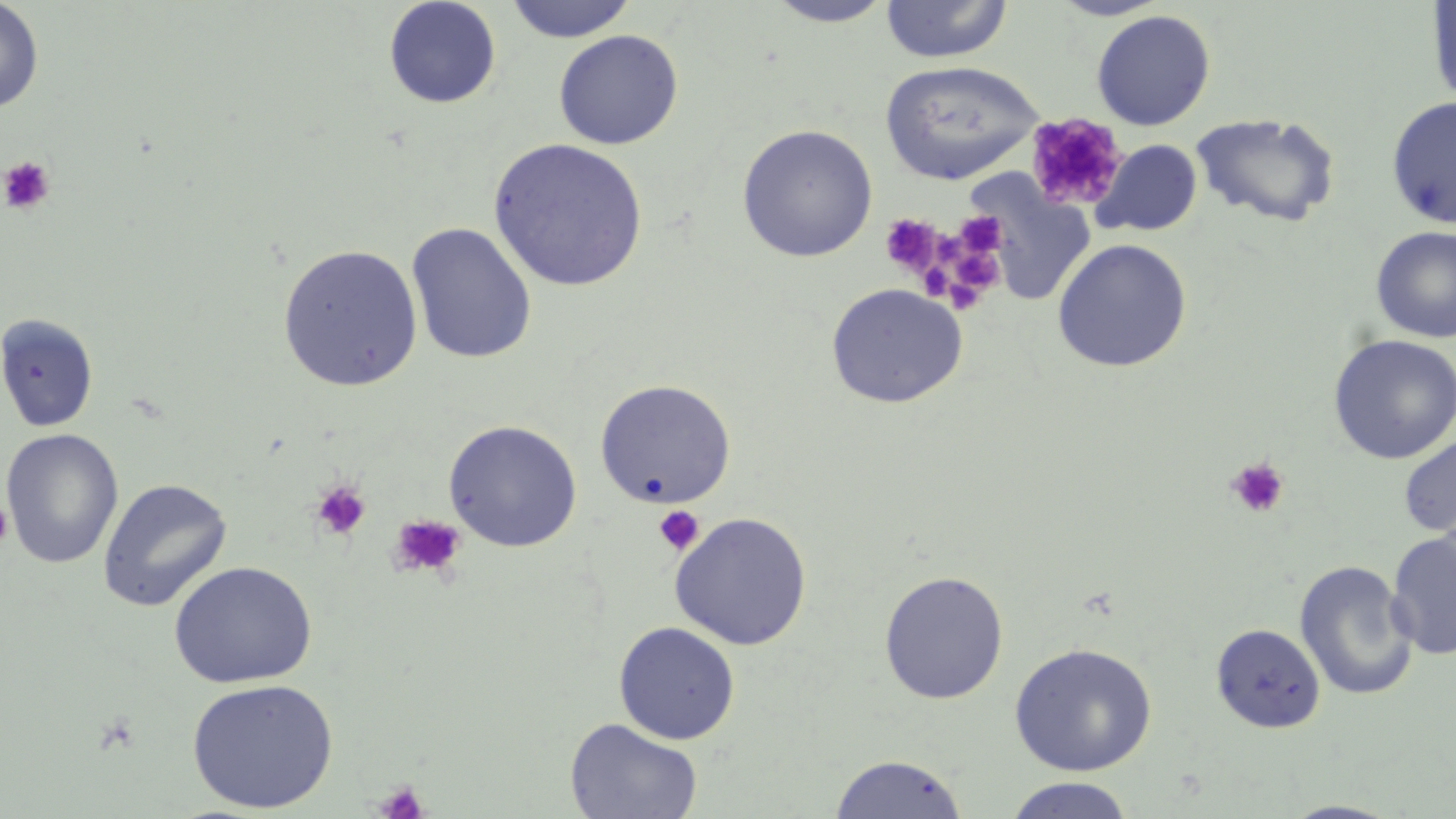
slide_level_diagnosis: negative for blood parasites
field_of_view: single
stain: May-Grünwald-Giemsa
magnification: 1000x
platelet_locations: 'approximate bounding boxes as (x1, y1, x2, y2) in pixels: (1026, 112, 1128, 213), (1, 157, 55, 216), (956, 211, 1005, 255), (879, 215, 944, 277), (935, 234, 966, 267), (959, 253, 1005, 298), (921, 262, 950, 299), (947, 271, 979, 315), (1226, 457, 1290, 518), (309, 480, 371, 541), (1, 497, 15, 553), (654, 505, 705, 555), (388, 513, 466, 579), (373, 781, 430, 819)'
uninfected_red_blood_cell_locations: 'approximate bounding boxes as (x1, y1, x2, y2) in pixels: (382, 0, 502, 109), (764, 0, 898, 27), (879, 0, 1014, 63), (1049, 0, 1171, 20), (1426, 0, 1456, 108), (0, 1, 44, 112), (503, 1, 638, 43), (1090, 9, 1216, 130), (553, 29, 683, 150), (878, 60, 1044, 185), (1386, 96, 1456, 230), (1190, 111, 1341, 229), (736, 124, 878, 262), (489, 138, 647, 292), (1093, 139, 1202, 237), (406, 222, 538, 364), (1371, 226, 1456, 343), (1052, 238, 1193, 373), (277, 244, 423, 392), (825, 283, 967, 408), (0, 313, 99, 433), (1327, 334, 1456, 464), (594, 379, 736, 508), (443, 420, 582, 551), (1, 428, 123, 569), (1398, 431, 1456, 541), (97, 478, 232, 612), (670, 511, 813, 650), (1386, 530, 1456, 660), (1294, 559, 1419, 701), (168, 561, 318, 689), (878, 570, 1009, 704), (613, 621, 740, 744), (1211, 623, 1326, 733), (1009, 642, 1158, 777), (185, 678, 338, 813), (564, 717, 703, 819), (829, 753, 970, 818), (1003, 776, 1136, 818), (1277, 799, 1407, 818)'
image_size: 1456×819 pixels
preparation: thin blood film
modality: light microscopy